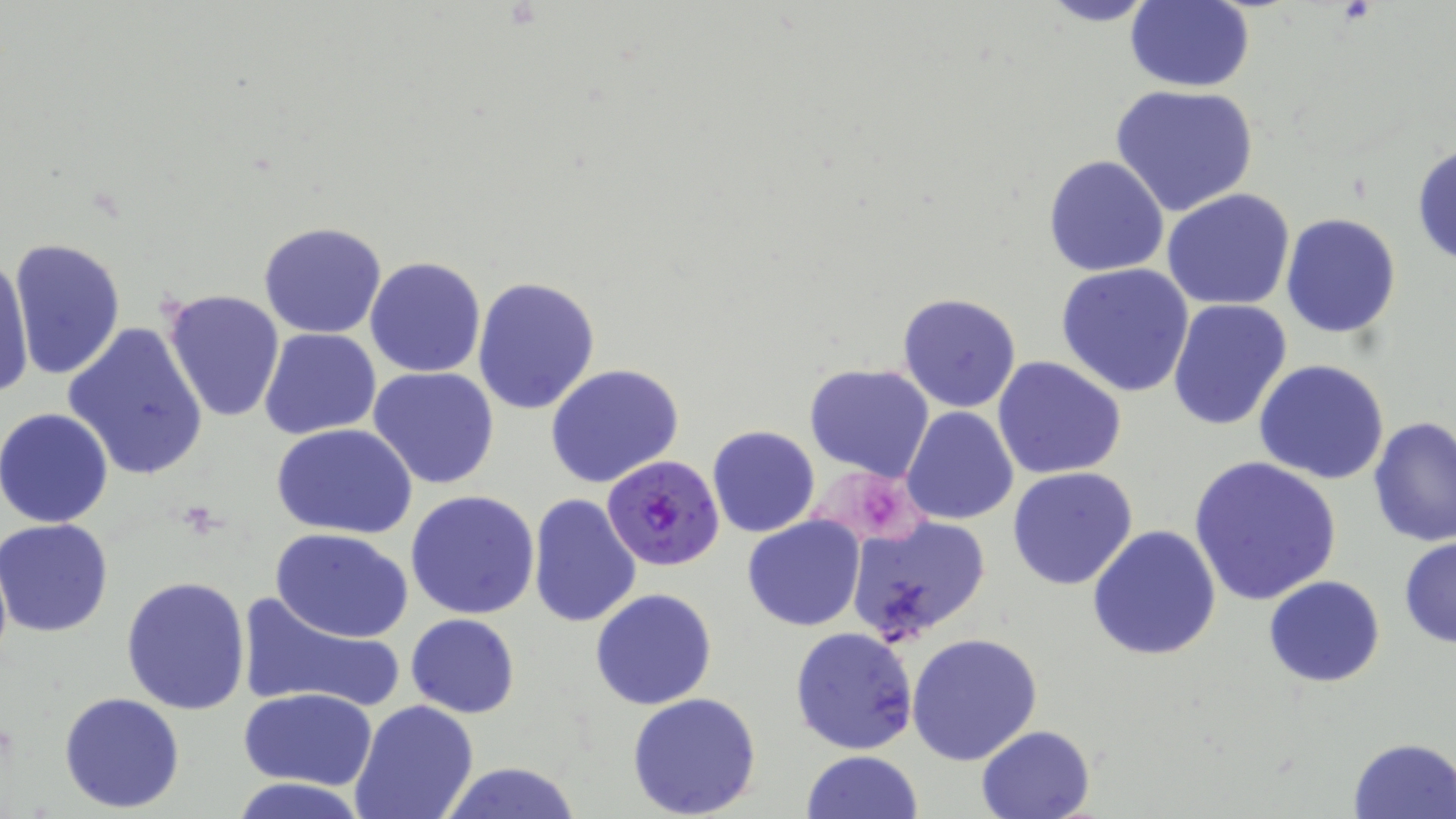
slide-level diagnosis = Plasmodium falciparum
magnification = 1000x
uninfected red blood cell locations = approximate bounding boxes as [x1, y1, x2, y2] in pixels: [1032, 0, 1164, 27], [1124, 1, 1255, 93], [1108, 84, 1260, 216], [1411, 142, 1456, 268], [1044, 154, 1168, 277], [1162, 189, 1296, 311], [1280, 212, 1402, 340], [259, 221, 388, 338], [8, 237, 127, 381], [1, 250, 36, 397], [364, 256, 485, 379], [1056, 263, 1198, 398], [471, 277, 600, 415], [161, 287, 285, 426], [897, 292, 1021, 412], [1167, 299, 1293, 431], [61, 322, 209, 480], [260, 327, 381, 439], [992, 356, 1128, 479], [1253, 360, 1391, 484], [545, 364, 685, 489], [804, 364, 935, 482], [368, 367, 500, 490], [900, 407, 1018, 526], [1, 408, 116, 527], [1368, 416, 1455, 548], [271, 423, 418, 539], [708, 428, 821, 537], [1188, 456, 1342, 605], [1008, 466, 1139, 590], [406, 490, 540, 618], [527, 492, 641, 630], [742, 514, 867, 632], [845, 515, 991, 648], [0, 519, 117, 637], [1087, 525, 1221, 663], [272, 529, 413, 642], [1398, 536, 1456, 650], [1263, 575, 1386, 688], [121, 576, 253, 715], [590, 588, 717, 710], [237, 589, 407, 715], [405, 613, 520, 718], [790, 626, 919, 755], [907, 631, 1042, 766], [240, 687, 378, 790], [59, 692, 185, 811], [626, 692, 762, 818], [349, 701, 479, 819], [975, 725, 1096, 818], [1348, 737, 1456, 817], [801, 750, 923, 819], [437, 763, 584, 819], [231, 778, 368, 818]
platelet locations = approximate bounding boxes as [x1, y1, x2, y2] in pixels: [853, 485, 902, 536]
image size = 1456×819 pixels
field of view = one of a larger specimen
preparation = thin blood smear
stain = May-Grünwald-Giemsa
modality = optical microscopy
Plasmodium falciparum-infected red blood cell locations = approximate bounding boxes as [x1, y1, x2, y2] in pixels: [603, 453, 724, 571]